Classify this cell by malaria status.
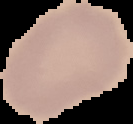
It is uninfected.

Image is 133×124 pixels. The area outside the segmented cell region is set to black. From a thin blood smear.